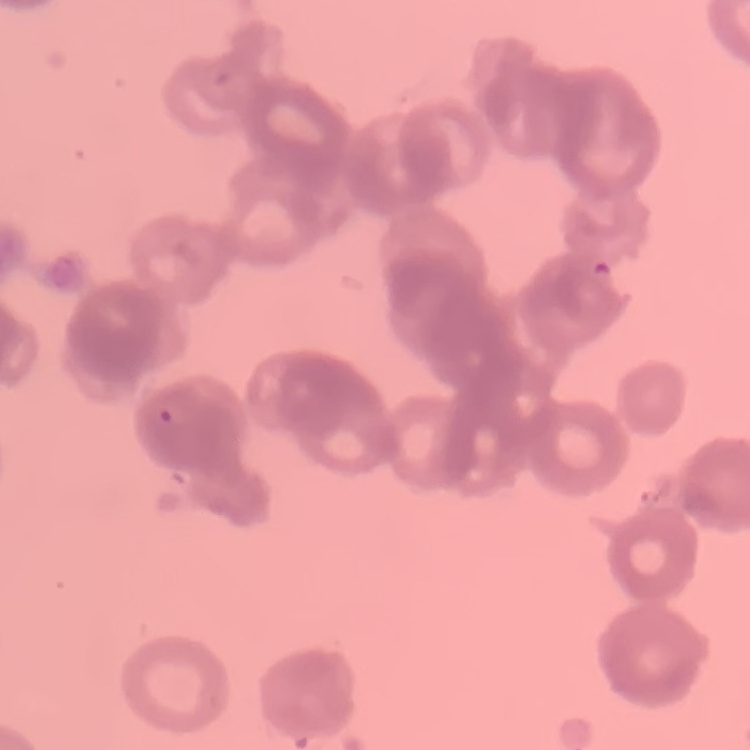

Summary:
  - Red blood cell morphology: rouleaux formation
  - Preparation: thin blood smear
  - Stain: Field's or Giemsa
  - Image type: one tile cut from a larger photomicrograph